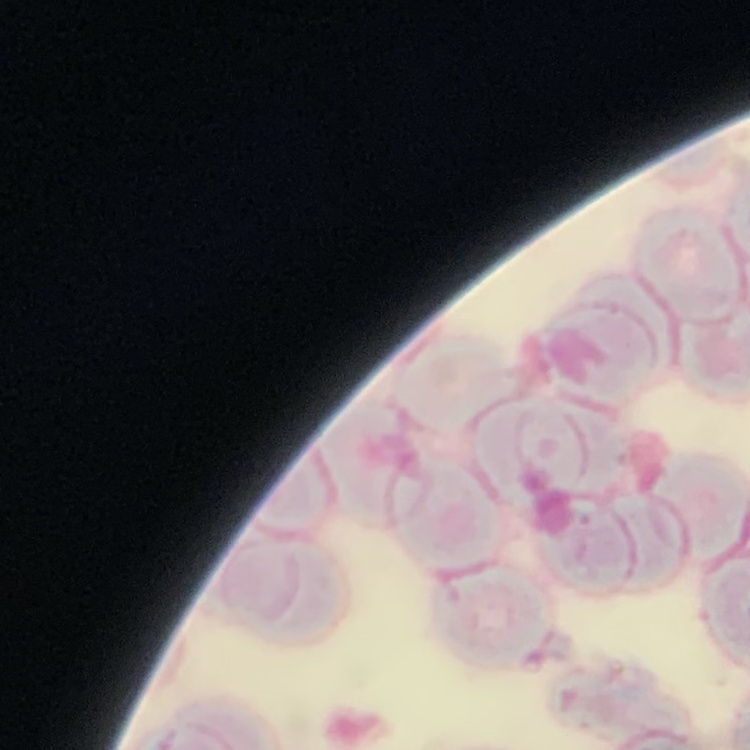
erythrocyte morphology = rouleaux formation
preparation = thin blood film
stain = Field's or Giemsa
image type = square crop of a larger photomicrograph